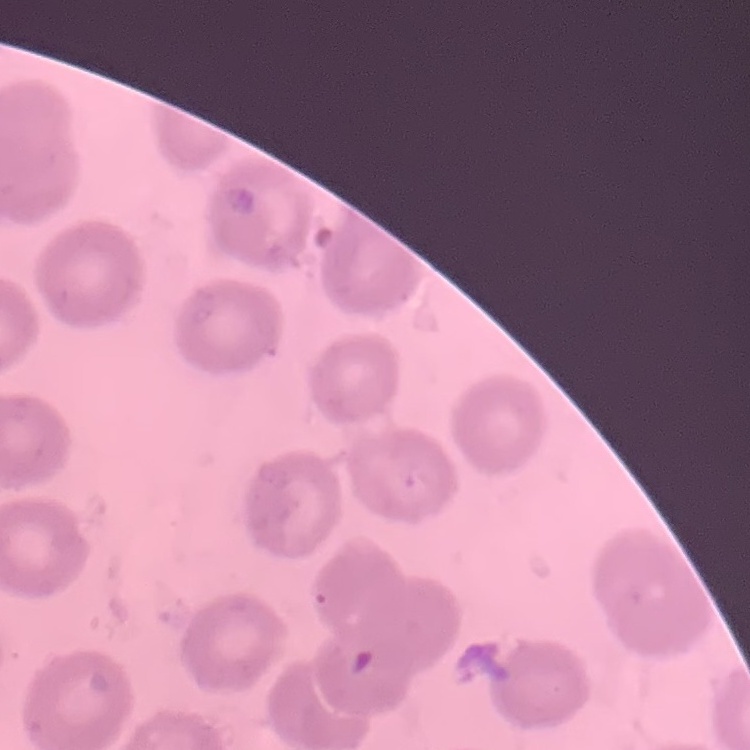

The red blood cells show no rouleaux formation. Thin peripheral smear. Field's or Giemsa stain. Square crop of a larger photomicrograph.